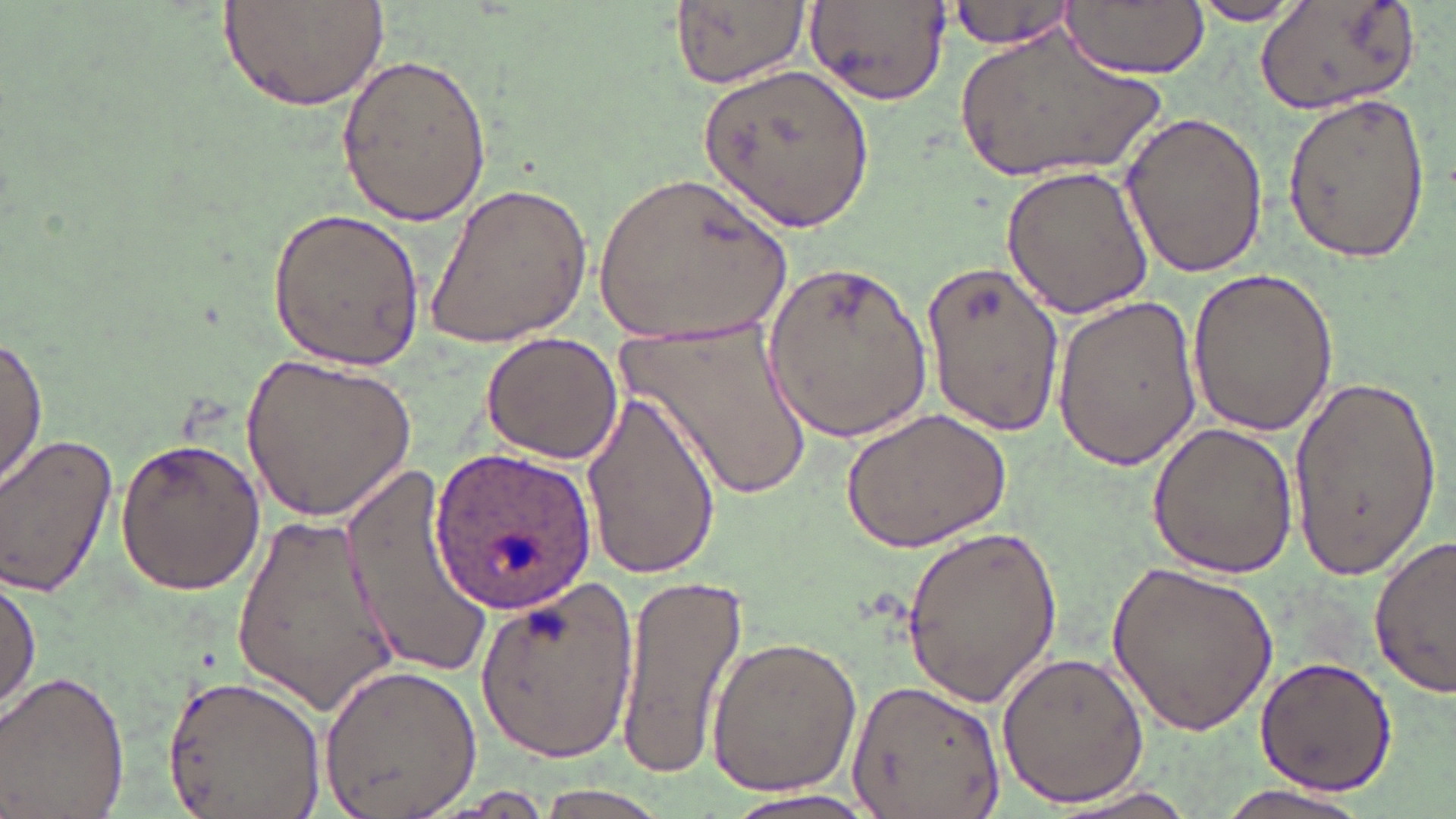
slide-level diagnosis = Plasmodium ovale
uninfected red blood cell locations = approximate bounding boxes as named x1/y1/x2/y2 corners in pixels: (x1=216, y1=0, x2=388, y2=110), (x1=803, y1=0, x2=950, y2=110), (x1=946, y1=0, x2=1078, y2=52), (x1=1061, y1=0, x2=1208, y2=78), (x1=1183, y1=0, x2=1312, y2=25), (x1=669, y1=1, x2=807, y2=88), (x1=1254, y1=2, x2=1429, y2=117), (x1=951, y1=26, x2=1173, y2=189), (x1=334, y1=53, x2=492, y2=227), (x1=699, y1=64, x2=874, y2=234), (x1=1280, y1=90, x2=1432, y2=266), (x1=1119, y1=108, x2=1269, y2=282), (x1=999, y1=165, x2=1156, y2=320), (x1=593, y1=174, x2=794, y2=346), (x1=424, y1=182, x2=590, y2=349), (x1=269, y1=206, x2=426, y2=374), (x1=763, y1=257, x2=933, y2=444), (x1=922, y1=261, x2=1062, y2=436), (x1=1187, y1=266, x2=1342, y2=437), (x1=1053, y1=292, x2=1203, y2=474), (x1=617, y1=313, x2=813, y2=502), (x1=480, y1=330, x2=624, y2=465), (x1=0, y1=333, x2=47, y2=497), (x1=241, y1=351, x2=416, y2=523), (x1=1283, y1=368, x2=1440, y2=578), (x1=580, y1=386, x2=722, y2=583), (x1=841, y1=408, x2=1012, y2=551), (x1=1145, y1=423, x2=1299, y2=579), (x1=0, y1=432, x2=119, y2=598), (x1=114, y1=435, x2=267, y2=595), (x1=342, y1=463, x2=492, y2=685), (x1=232, y1=509, x2=402, y2=716), (x1=900, y1=521, x2=1064, y2=710), (x1=1369, y1=534, x2=1456, y2=701), (x1=1107, y1=561, x2=1279, y2=733), (x1=615, y1=566, x2=748, y2=784), (x1=1, y1=576, x2=40, y2=718), (x1=473, y1=577, x2=642, y2=759), (x1=704, y1=635, x2=861, y2=797), (x1=996, y1=651, x2=1149, y2=809), (x1=1254, y1=655, x2=1396, y2=796), (x1=318, y1=660, x2=480, y2=819), (x1=1, y1=671, x2=133, y2=817), (x1=162, y1=673, x2=325, y2=819), (x1=845, y1=676, x2=1004, y2=818), (x1=1042, y1=784, x2=1208, y2=818), (x1=1210, y1=785, x2=1374, y2=818), (x1=526, y1=787, x2=675, y2=817), (x1=718, y1=787, x2=879, y2=819)
Plasmodium ovale-infected red blood cell locations = approximate bounding boxes as named x1/y1/x2/y2 corners in pixels: (x1=429, y1=449, x2=599, y2=607)
stain = May-Grünwald-Giemsa
preparation = thin blood film
field of view = one of a larger specimen
image size = 1456×819 pixels
modality = light microscopy
magnification = 1000x